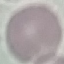
Summary:
  - Malaria status: uninfected
  - Stain: Giemsa
  - Image type: cell patch, automatically extracted from a larger field of view and resized to 64 × 64 pixels
  - Capture: smartphone camera at the microscope eyepiece
  - Preparation: thin smear